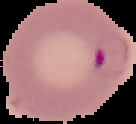

From a thin blood film. Malaria status: parasitized. Image is 136×124 pixels. Segmented cell region on a black background.